Report the malaria status of this cell.
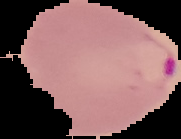
Parasitized.

From a thin blood film. Cell region segmented out of the field of view; the surrounding area is masked to black. Image is 181×139 pixels.